Report the malaria status of this cell.
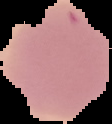

It is uninfected.

{
  "image_type": "cell region segmented out of the field of view; surrounding area masked to black",
  "image_size": "112×124 pixels",
  "preparation": "thin blood film"
}